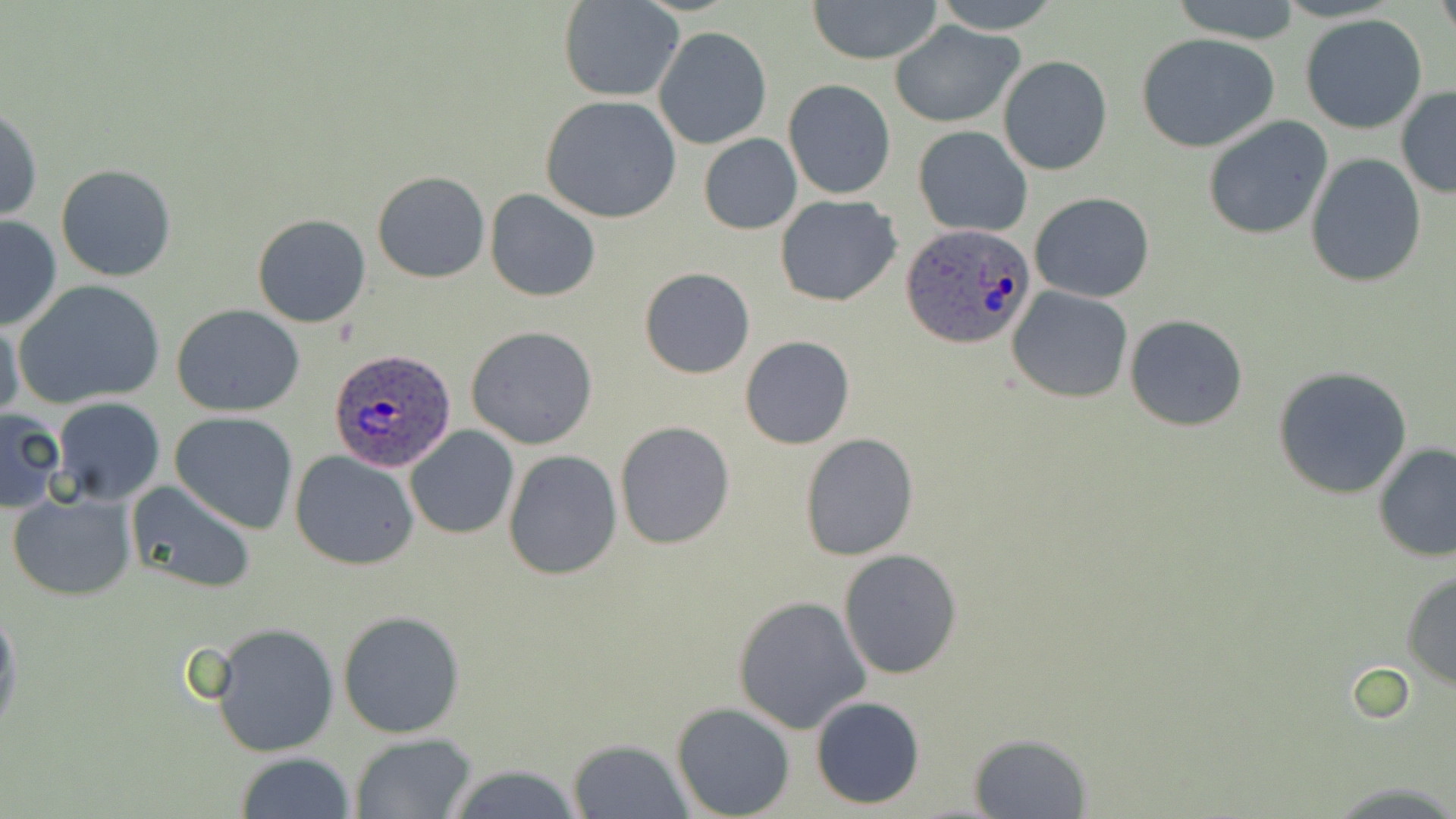 Approximate bounding boxes as [x1, y1, x2, y2] in pixels. Uninfected red blood cell locations: [807, 0, 944, 64], [931, 0, 1061, 33], [1169, 0, 1303, 43], [1437, 0, 1455, 39], [559, 1, 685, 102], [1300, 14, 1428, 135], [890, 21, 1024, 127], [654, 27, 771, 149], [1135, 33, 1280, 153], [997, 55, 1112, 176], [784, 79, 895, 200], [1395, 86, 1456, 197], [540, 95, 683, 224], [0, 107, 42, 222], [1201, 115, 1334, 241], [913, 125, 1034, 238], [698, 133, 802, 235], [1306, 154, 1428, 288], [56, 164, 177, 281], [372, 170, 490, 283], [484, 189, 601, 303], [1029, 191, 1155, 303], [775, 194, 903, 307], [252, 213, 373, 328], [0, 216, 62, 331], [640, 268, 754, 378], [14, 279, 165, 411], [1008, 286, 1133, 403], [173, 304, 305, 416], [1125, 314, 1248, 432], [0, 318, 25, 424], [466, 326, 599, 451], [739, 335, 854, 450], [1273, 367, 1414, 500], [37, 392, 154, 595], [52, 398, 165, 507], [1, 409, 65, 514], [170, 411, 299, 534], [615, 420, 735, 549], [405, 425, 520, 541], [799, 433, 918, 561], [1373, 444, 1456, 562], [290, 450, 420, 570], [502, 450, 623, 580], [125, 482, 256, 592], [8, 490, 136, 601], [838, 550, 963, 679], [1400, 571, 1456, 688], [732, 596, 870, 734], [0, 601, 21, 741], [337, 609, 466, 739], [207, 622, 343, 759], [811, 696, 926, 808], [671, 702, 794, 818], [351, 733, 476, 817], [968, 733, 1093, 819], [568, 738, 693, 817], [233, 751, 356, 819], [442, 765, 589, 819]. Plasmodium ovale-infected red blood cell locations: [901, 223, 1035, 352], [328, 347, 457, 473]. Slide-level diagnosis: Plasmodium ovale. Thin blood film. One field of a larger specimen. Light microscopy. May-Grünwald-Giemsa-stained preparation. 1000x magnification. Image is 1456×819 pixels.